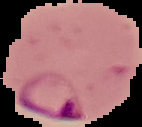

Summary:
  - Image size: 142×127 pixels
  - Result: Plasmodium parasites detected
  - Image type: segmented cell region with the area outside set to black
  - Preparation: thin blood smear